Assess this cell for malaria.
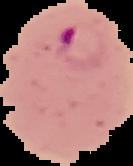
Parasitized.

The area outside the segmented cell region is set to black. Image is 133×166 pixels. From a thin blood film.